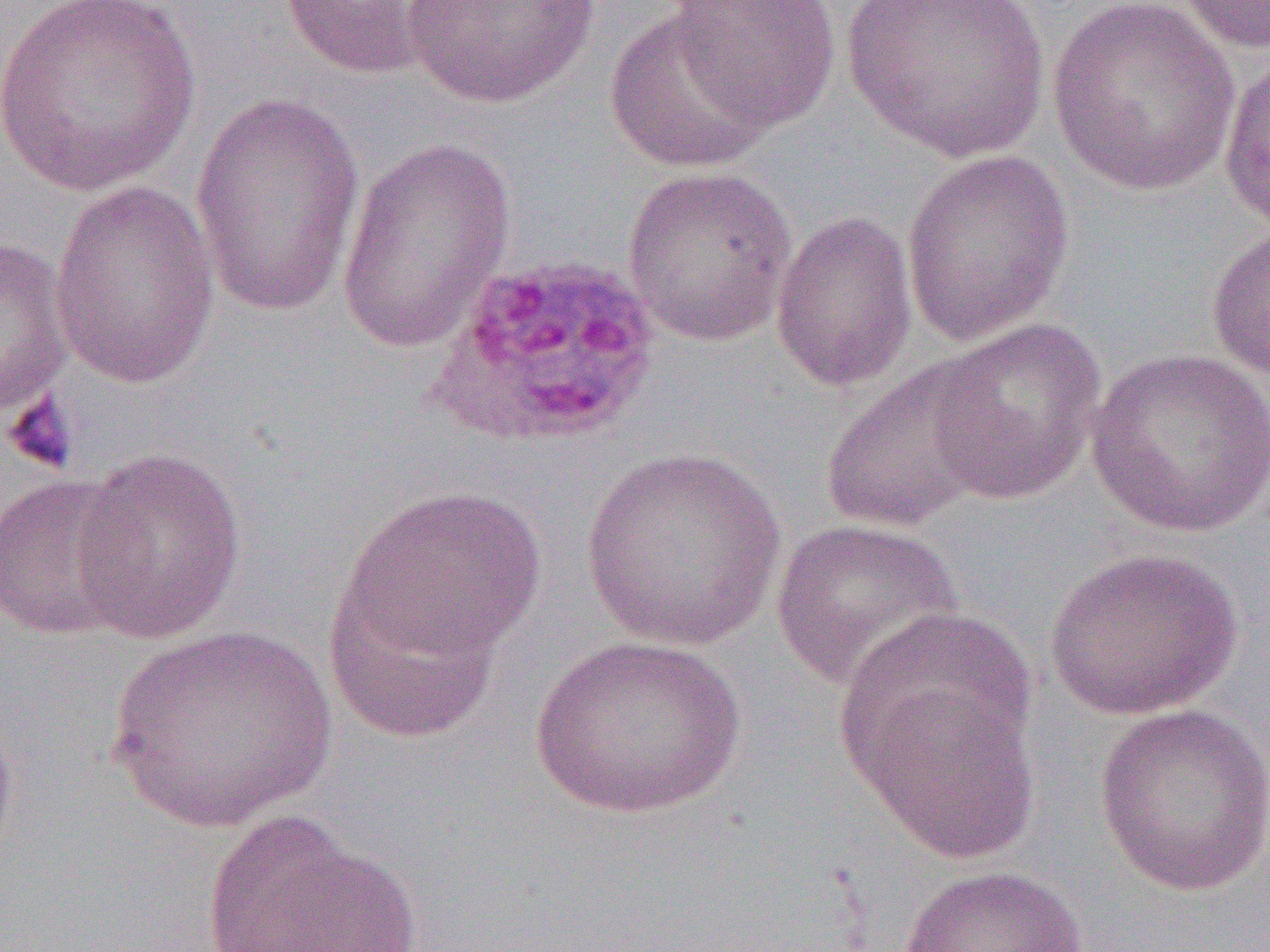 Approximate bounding boxes as named x1/y1/x2/y2 corners in pixels. Platelet locations: (x1=1, y1=389, x2=81, y2=476). Uninfected red blood cell locations: (x1=1, y1=0, x2=203, y2=196), (x1=277, y1=0, x2=452, y2=80), (x1=396, y1=0, x2=609, y2=110), (x1=841, y1=0, x2=1051, y2=165), (x1=1173, y1=0, x2=1270, y2=56), (x1=666, y1=1, x2=844, y2=131), (x1=1045, y1=1, x2=1243, y2=198), (x1=603, y1=7, x2=776, y2=175), (x1=1217, y1=52, x2=1270, y2=237), (x1=189, y1=93, x2=365, y2=317), (x1=335, y1=137, x2=516, y2=354), (x1=900, y1=148, x2=1076, y2=346), (x1=621, y1=165, x2=799, y2=347), (x1=48, y1=181, x2=221, y2=389), (x1=769, y1=207, x2=918, y2=394), (x1=1205, y1=223, x2=1270, y2=384), (x1=0, y1=235, x2=74, y2=427), (x1=927, y1=317, x2=1107, y2=505), (x1=1085, y1=346, x2=1270, y2=539), (x1=818, y1=357, x2=999, y2=535), (x1=68, y1=448, x2=247, y2=645), (x1=578, y1=448, x2=788, y2=651), (x1=0, y1=473, x2=143, y2=640), (x1=336, y1=484, x2=547, y2=665), (x1=771, y1=518, x2=963, y2=692), (x1=1044, y1=547, x2=1243, y2=721), (x1=322, y1=560, x2=509, y2=744), (x1=106, y1=625, x2=335, y2=831), (x1=528, y1=633, x2=748, y2=820), (x1=846, y1=662, x2=1043, y2=864), (x1=0, y1=698, x2=18, y2=880), (x1=1093, y1=702, x2=1270, y2=897), (x1=199, y1=808, x2=422, y2=952), (x1=897, y1=864, x2=1090, y2=951). Slide-level diagnosis: Plasmodium ovale. Thin blood smear. Image is 1270×952 pixels. Captured at 1000x magnification. One field of a larger specimen. Light microscopy.